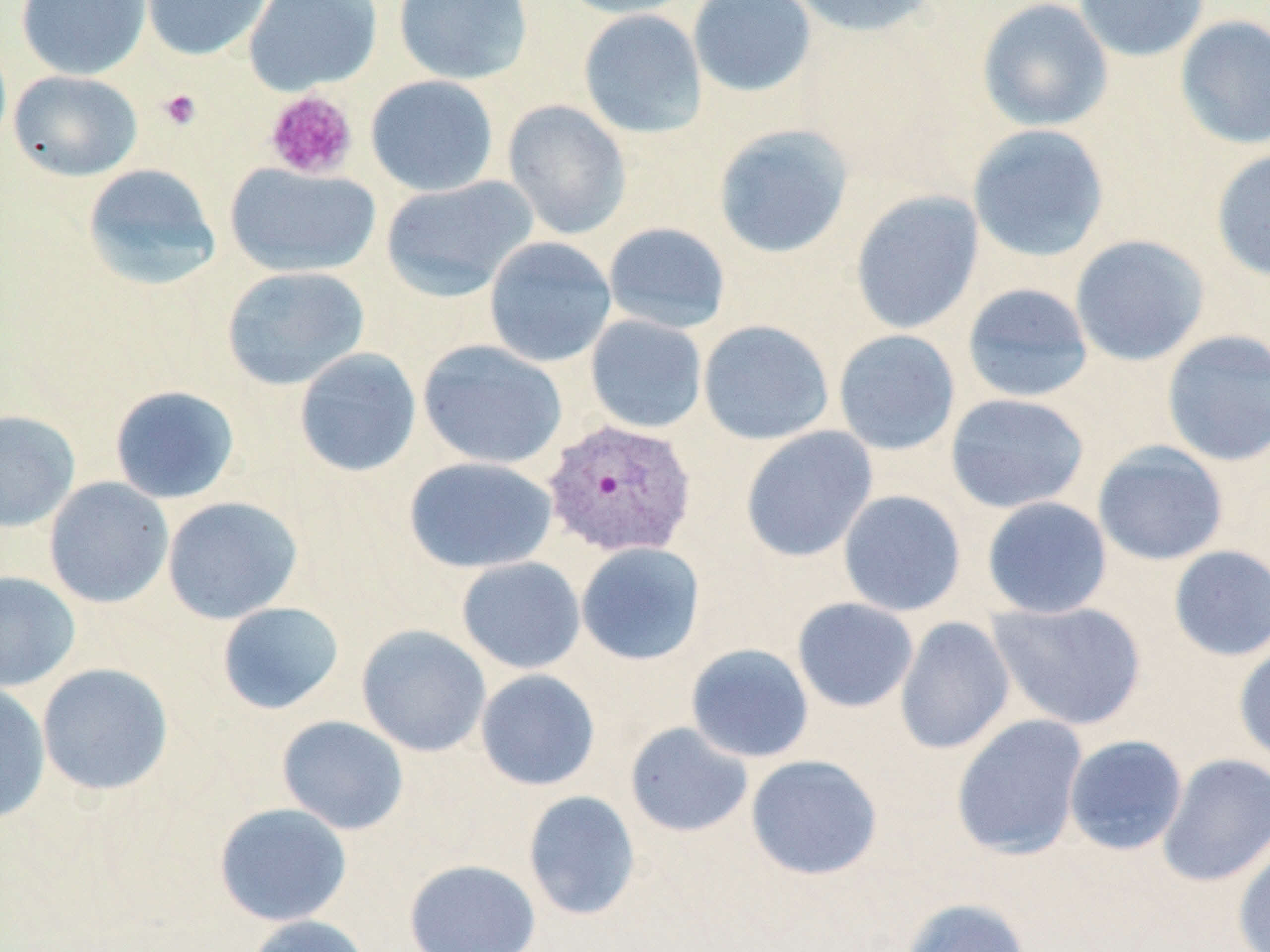
Summary:
  - Coordinate format: approximate bounding boxes as named x1/y1/x2/y2 corners in pixels
  - Plasmodium vivax-infected red blood cell locations: (x1=542, y1=418, x2=698, y2=558)
  - Platelet locations: (x1=157, y1=89, x2=202, y2=131), (x1=263, y1=90, x2=358, y2=180)
  - Uninfected red blood cell locations: (x1=15, y1=0, x2=151, y2=81), (x1=141, y1=0, x2=274, y2=61), (x1=244, y1=0, x2=382, y2=95), (x1=393, y1=0, x2=532, y2=85), (x1=556, y1=0, x2=698, y2=19), (x1=687, y1=0, x2=817, y2=99), (x1=785, y1=0, x2=940, y2=38), (x1=976, y1=0, x2=1113, y2=132), (x1=1073, y1=0, x2=1211, y2=62), (x1=578, y1=9, x2=708, y2=139), (x1=1174, y1=14, x2=1270, y2=150), (x1=8, y1=70, x2=142, y2=181), (x1=365, y1=75, x2=499, y2=197), (x1=502, y1=100, x2=632, y2=240), (x1=712, y1=123, x2=855, y2=260), (x1=967, y1=124, x2=1110, y2=263), (x1=1210, y1=148, x2=1270, y2=283), (x1=225, y1=162, x2=381, y2=278), (x1=82, y1=163, x2=222, y2=291), (x1=380, y1=175, x2=538, y2=302), (x1=850, y1=191, x2=985, y2=335), (x1=602, y1=222, x2=732, y2=334), (x1=1069, y1=234, x2=1210, y2=367), (x1=483, y1=236, x2=617, y2=368), (x1=221, y1=265, x2=370, y2=391), (x1=961, y1=283, x2=1094, y2=403), (x1=585, y1=315, x2=707, y2=434), (x1=698, y1=320, x2=834, y2=445), (x1=833, y1=329, x2=961, y2=456), (x1=1160, y1=329, x2=1270, y2=467), (x1=417, y1=339, x2=567, y2=470), (x1=293, y1=347, x2=422, y2=477), (x1=109, y1=385, x2=241, y2=504), (x1=945, y1=393, x2=1090, y2=514), (x1=0, y1=409, x2=80, y2=533), (x1=740, y1=426, x2=878, y2=562), (x1=1092, y1=441, x2=1230, y2=566), (x1=403, y1=456, x2=557, y2=574), (x1=43, y1=477, x2=174, y2=609), (x1=837, y1=489, x2=966, y2=617), (x1=161, y1=496, x2=302, y2=624), (x1=982, y1=496, x2=1113, y2=619), (x1=575, y1=542, x2=706, y2=666), (x1=1167, y1=545, x2=1270, y2=662), (x1=456, y1=557, x2=586, y2=674), (x1=0, y1=571, x2=81, y2=692), (x1=792, y1=597, x2=918, y2=713), (x1=987, y1=599, x2=1148, y2=731), (x1=216, y1=601, x2=345, y2=715), (x1=894, y1=616, x2=1015, y2=755), (x1=356, y1=625, x2=491, y2=757), (x1=1234, y1=641, x2=1270, y2=766), (x1=686, y1=643, x2=814, y2=763), (x1=36, y1=662, x2=174, y2=796), (x1=475, y1=669, x2=601, y2=791), (x1=0, y1=684, x2=51, y2=825), (x1=950, y1=714, x2=1088, y2=860), (x1=277, y1=715, x2=409, y2=835), (x1=625, y1=721, x2=754, y2=838), (x1=1063, y1=734, x2=1188, y2=856), (x1=1157, y1=753, x2=1270, y2=887), (x1=745, y1=754, x2=883, y2=880), (x1=522, y1=790, x2=641, y2=921), (x1=214, y1=802, x2=352, y2=927), (x1=1233, y1=833, x2=1270, y2=952), (x1=403, y1=858, x2=541, y2=952), (x1=900, y1=897, x2=1032, y2=952), (x1=244, y1=914, x2=374, y2=952)
  - Slide-level diagnosis: Plasmodium vivax
  - Preparation: thin blood film
  - Modality: light microscopy
  - Stain: May-Grünwald-Giemsa
  - Image size: 1270×952 pixels
  - Field of view: single
  - Magnification: 1000x